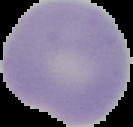 Image is 133×127 pixels. Cell region segmented out of the field of view; the surrounding area is masked to black. From a thin blood smear. Result: no malaria parasites seen.